Locate and identify every blood parasite.
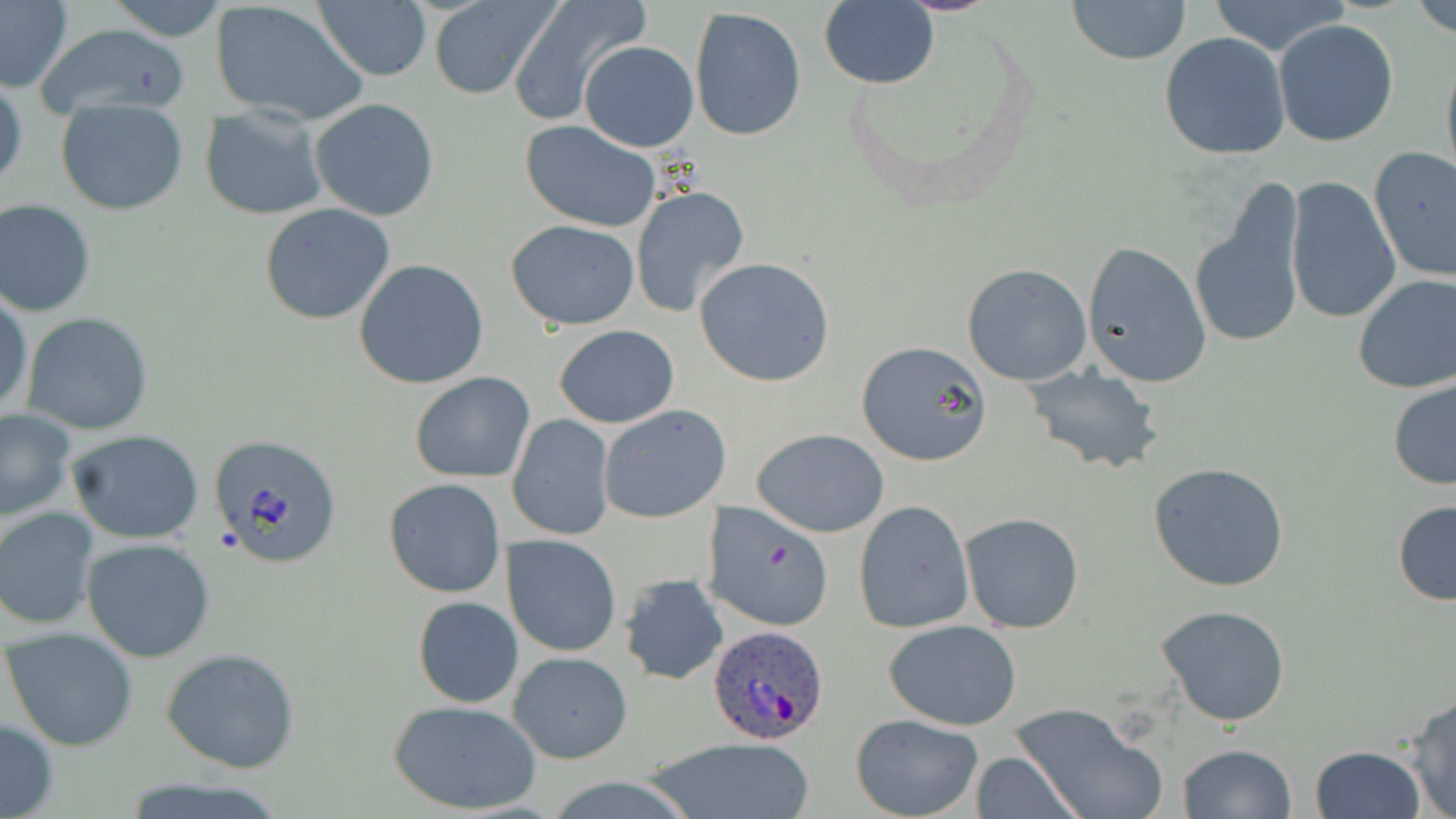
Approximate bounding boxes as [x1, y1, x2, y2] in pixels.
Plasmodium ovale-infected red blood cells: [707, 625, 833, 745].
No Plasmodium falciparum, Plasmodium malariae, Plasmodium vivax, Babesia divergens, or Trypanosoma brucei observed.

slide-level diagnosis = Plasmodium ovale
modality = optical microscopy
uninfected red blood cell locations = approximate bounding boxes as [x1, y1, x2, y2] in pixels: [0, 0, 74, 94], [105, 0, 228, 42], [507, 0, 649, 126], [820, 0, 940, 89], [1066, 0, 1191, 65], [1205, 0, 1354, 59], [1408, 0, 1456, 39], [211, 1, 368, 128], [428, 1, 557, 101], [315, 2, 432, 81], [689, 7, 809, 144], [1275, 19, 1398, 147], [33, 20, 191, 121], [1160, 34, 1290, 161], [579, 41, 699, 153], [1440, 47, 1456, 188], [1, 74, 26, 196], [310, 97, 440, 221], [55, 98, 189, 216], [18, 107, 155, 261], [201, 107, 326, 221], [519, 121, 662, 235], [1368, 147, 1456, 283], [1284, 176, 1401, 326], [630, 185, 752, 322], [0, 200, 97, 317], [260, 202, 395, 323], [1193, 207, 1304, 349], [506, 220, 640, 330], [1082, 243, 1210, 387], [693, 257, 835, 387], [354, 259, 490, 390], [962, 263, 1092, 385], [1352, 274, 1456, 394], [0, 290, 33, 418], [20, 311, 154, 435], [554, 324, 679, 427], [855, 341, 994, 466], [1021, 363, 1166, 477], [409, 372, 535, 484], [1386, 378, 1456, 490], [599, 405, 731, 523], [0, 409, 76, 521], [507, 414, 615, 541], [752, 428, 890, 537], [64, 429, 207, 545], [1148, 462, 1291, 593], [383, 478, 507, 599], [1392, 499, 1456, 605], [854, 501, 974, 633], [702, 502, 836, 634], [0, 506, 100, 630], [960, 512, 1084, 634], [504, 535, 621, 657], [82, 537, 216, 663], [618, 572, 729, 685], [412, 596, 524, 708], [1156, 604, 1292, 726], [883, 620, 1023, 731], [3, 627, 141, 752], [161, 646, 301, 773], [508, 651, 634, 764], [1402, 691, 1456, 818], [387, 698, 542, 816], [1008, 702, 1167, 819], [850, 713, 984, 819], [0, 716, 59, 818], [645, 735, 816, 819], [1176, 744, 1297, 819], [1309, 745, 1428, 819], [968, 752, 1084, 818], [116, 776, 292, 819]
image size = 1456×819 pixels
preparation = thin blood smear
stain = May-Grünwald-Giemsa
field of view = single
magnification = 1000x